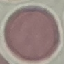
Result: no malaria parasites detected. Thin blood film. Giemsa stain. Cell patch, automatically extracted from a larger field of view and resized to 64 × 64 pixels. Photographed with a smartphone camera at the microscope eyepiece.